Give the extent of all Plasmodium falciparum-infected red blood cells.
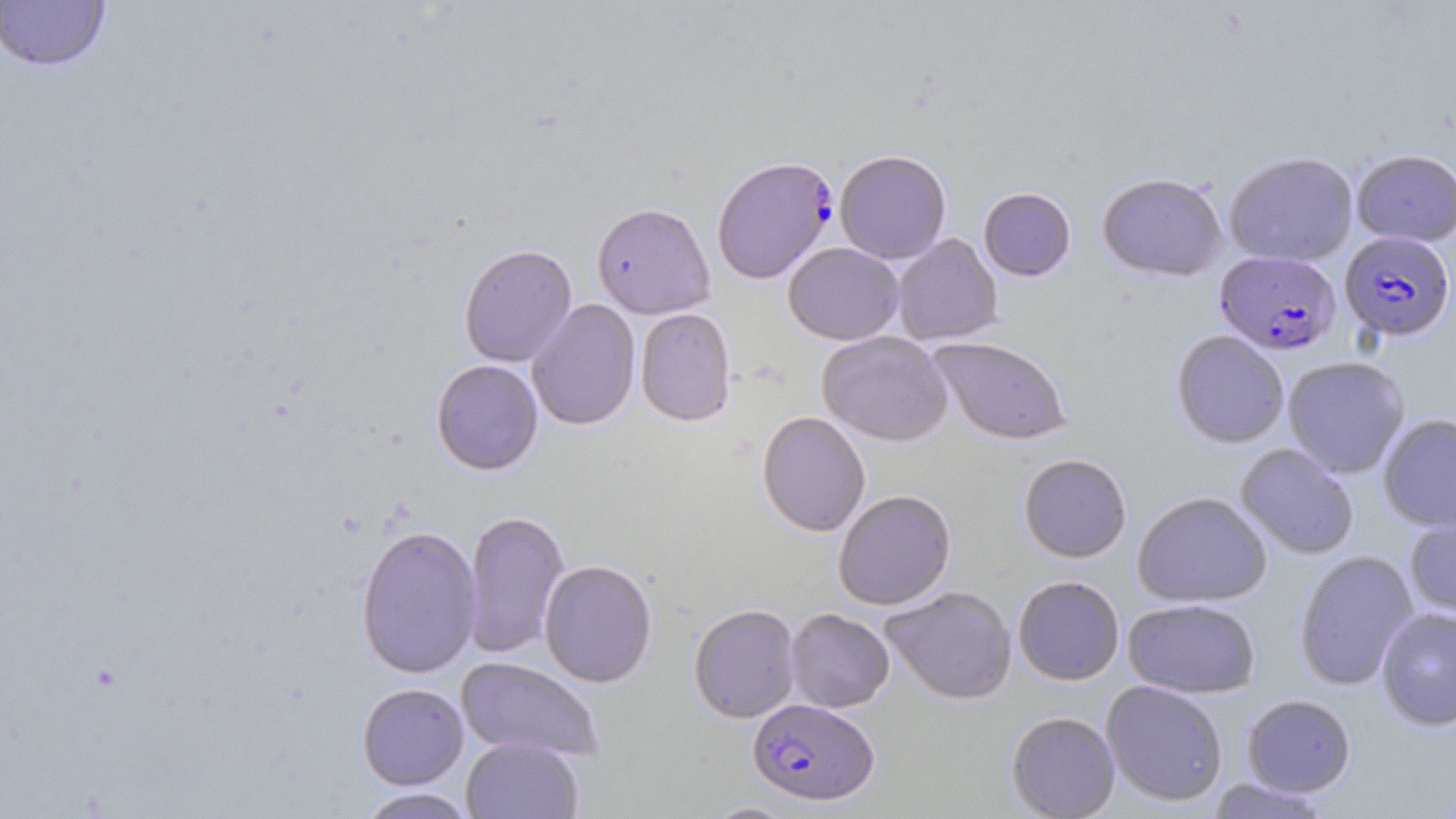

Approximate bounding boxes as (x1,y1)-(x2,y2) corner pairs in pixels.
Plasmodium falciparum-infected red blood cells: (715,159)-(841,288), (1340,232)-(1455,342), (1215,250)-(1341,355), (748,698)-(879,805).

{
  "slide_level_diagnosis": "Plasmodium falciparum",
  "modality": "light microscopy",
  "preparation": "thin blood film",
  "image_size": "1456×819 pixels",
  "field_of_view": "one of a larger specimen",
  "magnification": "1000x",
  "uninfected_red_blood_cell_locations": "approximate bounding boxes as (x1,y1)-(x2,y2) corner pairs in pixels: (0,1)-(113,73), (834,149)-(952,264), (1352,149)-(1456,246), (1224,151)-(1358,267), (1096,172)-(1227,281), (978,187)-(1076,281), (591,202)-(714,319), (893,234)-(1003,346), (783,242)-(904,345), (458,243)-(577,367), (526,299)-(641,431), (635,307)-(737,427), (1171,330)-(1289,449), (817,331)-(953,446), (927,337)-(1072,446), (1282,355)-(1411,479), (430,359)-(544,475), (756,411)-(870,537), (1377,413)-(1456,533), (1235,443)-(1359,560), (1019,453)-(1132,563), (833,490)-(956,610), (1132,491)-(1272,608), (463,509)-(570,661), (1403,514)-(1456,619), (355,523)-(483,679), (1293,550)-(1418,691), (539,559)-(657,688), (1012,575)-(1125,685), (881,586)-(1016,705), (1122,598)-(1261,699), (689,604)-(800,723), (1375,606)-(1456,731), (786,608)-(895,713), (456,656)-(604,762), (1101,680)-(1228,806), (357,683)-(469,790), (1241,694)-(1356,797), (1006,711)-(1120,818), (461,737)-(584,819), (1204,777)-(1334,818), (356,787)-(477,818), (702,802)-(800,818)",
  "stain": "May-Grünwald-Giemsa"
}